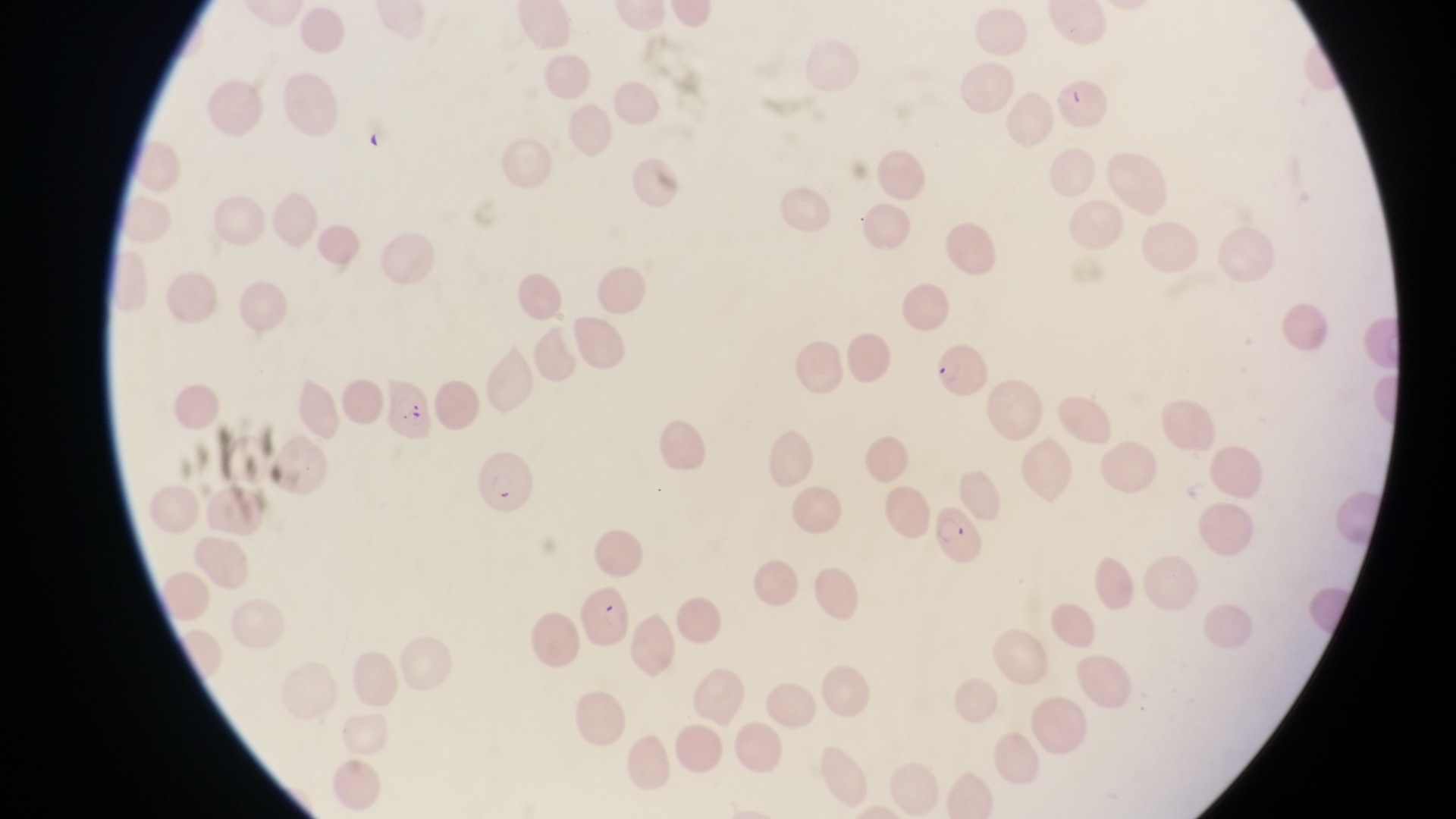

field of view = single
parasitised red blood cell locations = approximate bounding boxes as (left, top, right, bottom) in pixels: (935, 338, 995, 409), (378, 373, 439, 446), (476, 450, 539, 524), (931, 505, 984, 574), (581, 581, 633, 652)
preparation = thin blood smear
image size = 1456×819 pixels
capture = smartphone photograph through the eyepiece of an Olympus CX-23 microscope
magnification = 1000x
country = Uganda